State the blood parasite species.
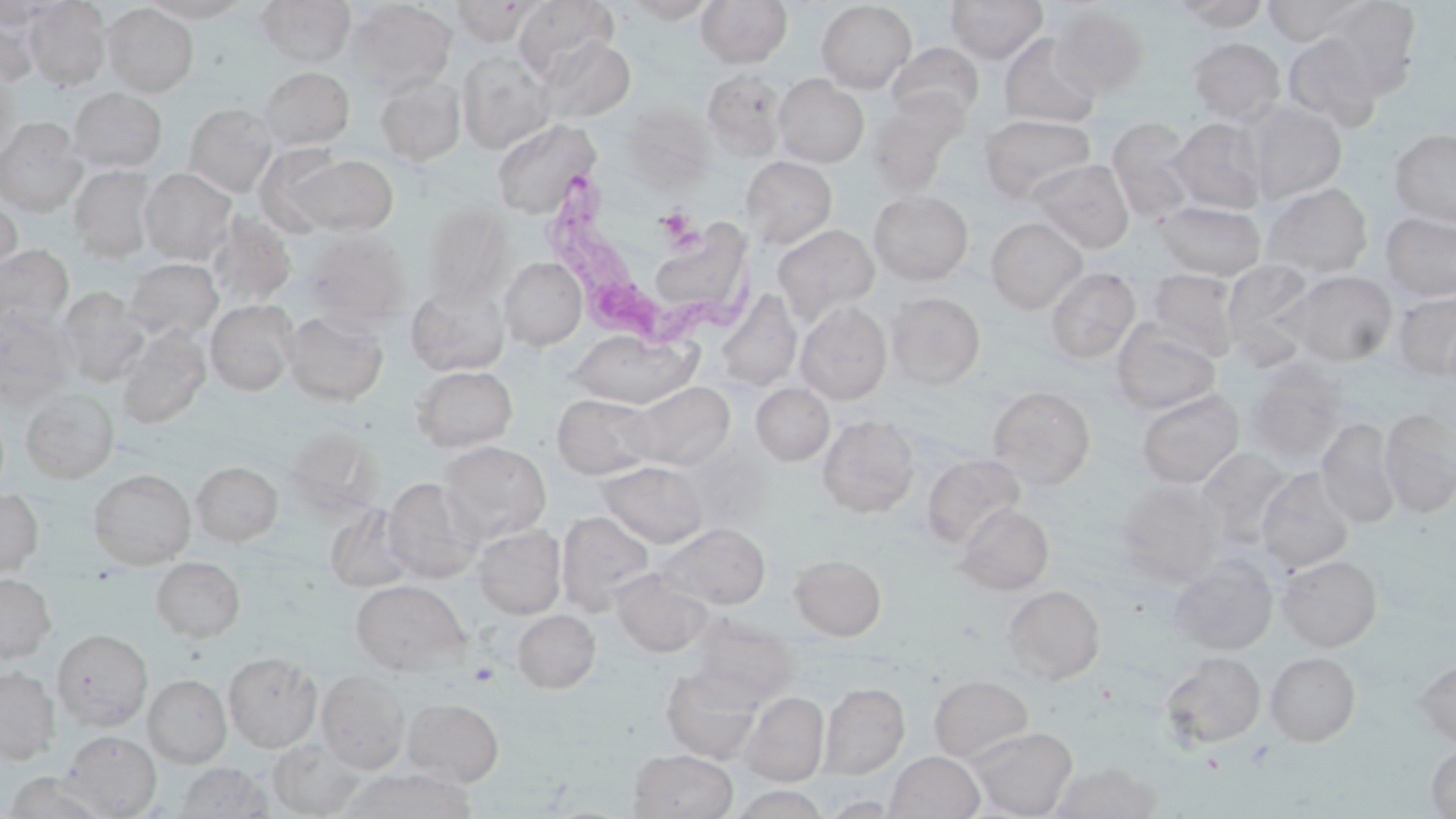
Trypanosoma brucei.

Summary:
  - Coordinate format: approximate bounding boxes as (x1, y1, x2, y2) in pixels
  - Trypanosoma brucei locations: (542, 171, 753, 357)
  - Uninfected red blood cell locations: (24, 0, 112, 90), (141, 0, 252, 22), (256, 0, 355, 66), (513, 0, 617, 80), (623, 0, 720, 23), (695, 0, 793, 68), (944, 0, 1048, 64), (1172, 0, 1271, 31), (1261, 0, 1370, 46), (1317, 0, 1422, 93), (0, 1, 71, 30), (343, 1, 458, 96), (449, 1, 538, 45), (815, 1, 917, 92), (101, 3, 199, 97), (1051, 6, 1149, 98), (0, 8, 41, 87), (998, 33, 1100, 128), (1281, 33, 1387, 132), (535, 36, 636, 125), (1188, 38, 1285, 123), (887, 43, 984, 123), (456, 53, 555, 154), (258, 66, 355, 150), (0, 68, 18, 159), (702, 70, 788, 161), (773, 75, 869, 167), (374, 76, 466, 166), (67, 88, 167, 173), (867, 96, 964, 195), (1242, 101, 1347, 202), (184, 103, 278, 196), (618, 104, 714, 190), (978, 114, 1096, 205), (0, 117, 86, 215), (1106, 117, 1198, 221), (1169, 117, 1270, 213), (492, 119, 600, 218), (1389, 128, 1456, 228), (290, 154, 398, 235), (741, 156, 837, 249), (1029, 159, 1134, 252), (69, 165, 158, 262), (139, 168, 237, 264), (1261, 183, 1373, 278), (868, 190, 974, 285), (878, 191, 978, 387), (0, 196, 22, 285), (1155, 200, 1266, 279), (422, 204, 514, 303), (656, 212, 753, 309), (1380, 212, 1456, 303), (205, 213, 296, 309), (986, 218, 1087, 312), (772, 223, 880, 321), (304, 229, 410, 325), (0, 244, 73, 332), (499, 257, 587, 351), (124, 258, 223, 343), (1221, 260, 1320, 362), (1045, 267, 1140, 364), (1146, 269, 1240, 358), (1283, 270, 1398, 366), (405, 281, 511, 377), (57, 288, 149, 387), (717, 289, 801, 392), (1391, 290, 1456, 383), (886, 291, 986, 389), (205, 299, 298, 396), (795, 301, 893, 405), (0, 307, 74, 407), (283, 309, 389, 406), (1111, 323, 1221, 415), (116, 329, 211, 429), (567, 329, 699, 409), (1244, 365, 1349, 465), (411, 366, 517, 452), (624, 381, 735, 471), (751, 383, 834, 465), (988, 385, 1096, 489), (21, 388, 119, 483), (1136, 390, 1244, 488), (552, 393, 657, 479), (1379, 408, 1456, 517), (817, 415, 920, 518), (1316, 419, 1401, 527), (441, 441, 551, 541), (1197, 448, 1296, 547), (922, 453, 1025, 549), (598, 461, 708, 548), (191, 462, 283, 546), (88, 468, 197, 569), (1256, 468, 1356, 573), (382, 477, 484, 583), (1116, 480, 1224, 584), (0, 489, 43, 578), (957, 503, 1054, 594), (324, 504, 416, 593), (556, 510, 655, 614), (658, 523, 770, 609), (472, 525, 566, 618), (789, 554, 887, 640), (1277, 555, 1382, 651), (1273, 556, 1368, 746), (151, 557, 245, 642), (1168, 557, 1277, 655), (610, 570, 714, 657), (0, 573, 56, 661), (351, 580, 469, 674), (1003, 585, 1105, 683), (513, 609, 600, 693), (689, 615, 798, 704), (53, 628, 153, 730), (1160, 651, 1266, 749), (223, 652, 322, 753), (1265, 652, 1360, 746), (1415, 657, 1456, 746), (660, 664, 766, 763), (0, 667, 60, 765), (316, 671, 408, 773), (143, 674, 232, 768), (929, 674, 1034, 763), (820, 682, 909, 779), (741, 692, 828, 785), (401, 698, 504, 786), (968, 726, 1078, 818), (61, 731, 162, 817), (268, 737, 365, 817), (1425, 742, 1456, 818), (628, 749, 738, 819), (886, 751, 985, 818), (176, 762, 272, 818), (1050, 762, 1161, 819), (339, 768, 477, 818), (5, 772, 110, 818), (729, 785, 832, 819)
  - Modality: optical microscopy
  - Preparation: thin blood film
  - Magnification: 1000x
  - Stain: May-Grünwald-Giemsa
  - Image size: 1456×819 pixels
  - Field of view: one of a larger specimen